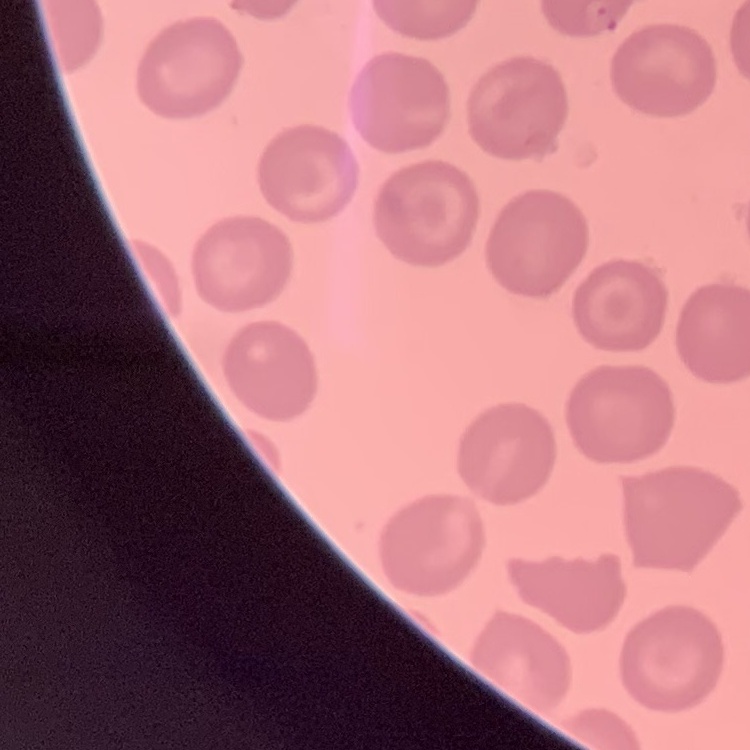
Summary:
  - Erythrocyte morphology: no rouleaux formation
  - Stain: Field's or Giemsa
  - Image type: square crop of a larger photomicrograph
  - Preparation: thin blood smear